Classify this cell by malaria status.
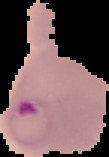
It is parasitized.

Summary:
  - Image size: 109×157 pixels
  - Image type: segmented cell region with the area outside set to black
  - Preparation: thin blood film